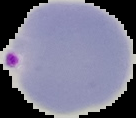
image_type: segmented cell region with the area outside set to black
preparation: thin blood film
malaria_status: parasitized
image_size: 136×118 pixels